Point out every Plasmodium parasite and every leukocyte.
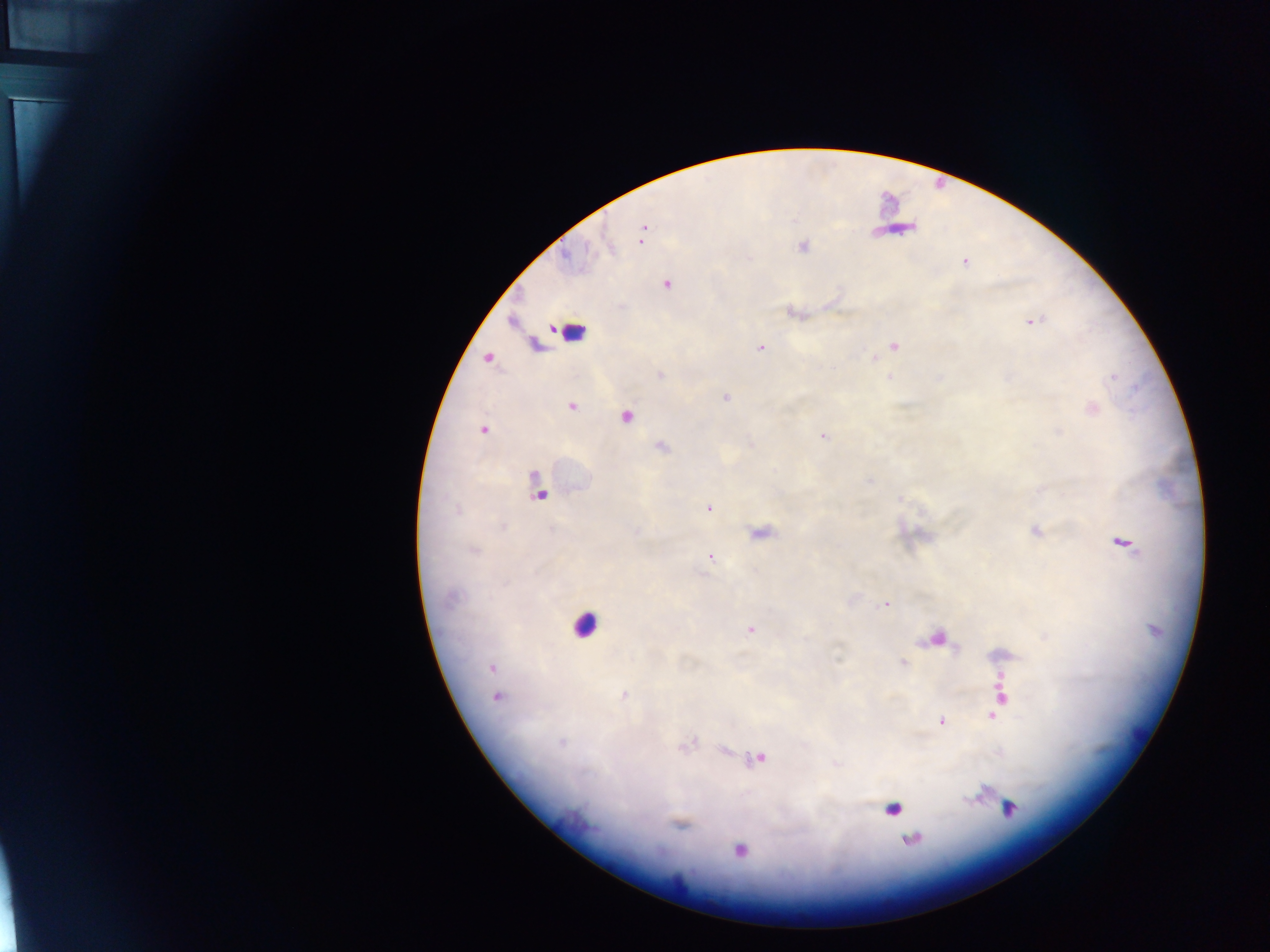

Approximate centers as [x, y] in pixels.
Plasmodium parasites: [642, 227], [641, 239], [802, 245], [964, 262], [666, 284], [1032, 321], [893, 345], [760, 346], [875, 358], [659, 375], [889, 376], [1113, 376], [725, 397], [572, 406], [626, 417], [482, 431], [1059, 431], [822, 435], [660, 447], [869, 481], [535, 487], [899, 498], [708, 506], [1037, 530], [762, 532], [1128, 542], [473, 550], [711, 558], [447, 597], [884, 604], [749, 630], [1046, 636], [941, 639], [1010, 654], [838, 660], [902, 663], [1003, 677], [624, 694], [496, 697], [1004, 698], [1000, 707], [995, 715], [942, 719], [560, 741], [693, 741], [687, 747], [758, 757], [967, 797], [1010, 808], [681, 824], [911, 838], [739, 851], [680, 877].
Leukocytes: [573, 335], [585, 625], [893, 807].

One field of view. Photographed through a microscope with a mobile-phone camera. Image is 1270×952 pixels. Sample from Ghana. Thick blood smear.